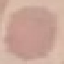 Malaria status: uninfected. Giemsa stain. Automatically extracted cell patch, resized to 64 × 64 pixels. Thin smear of blood. Acquired by smartphone through the microscope eyepiece.